Name the blood parasite species.
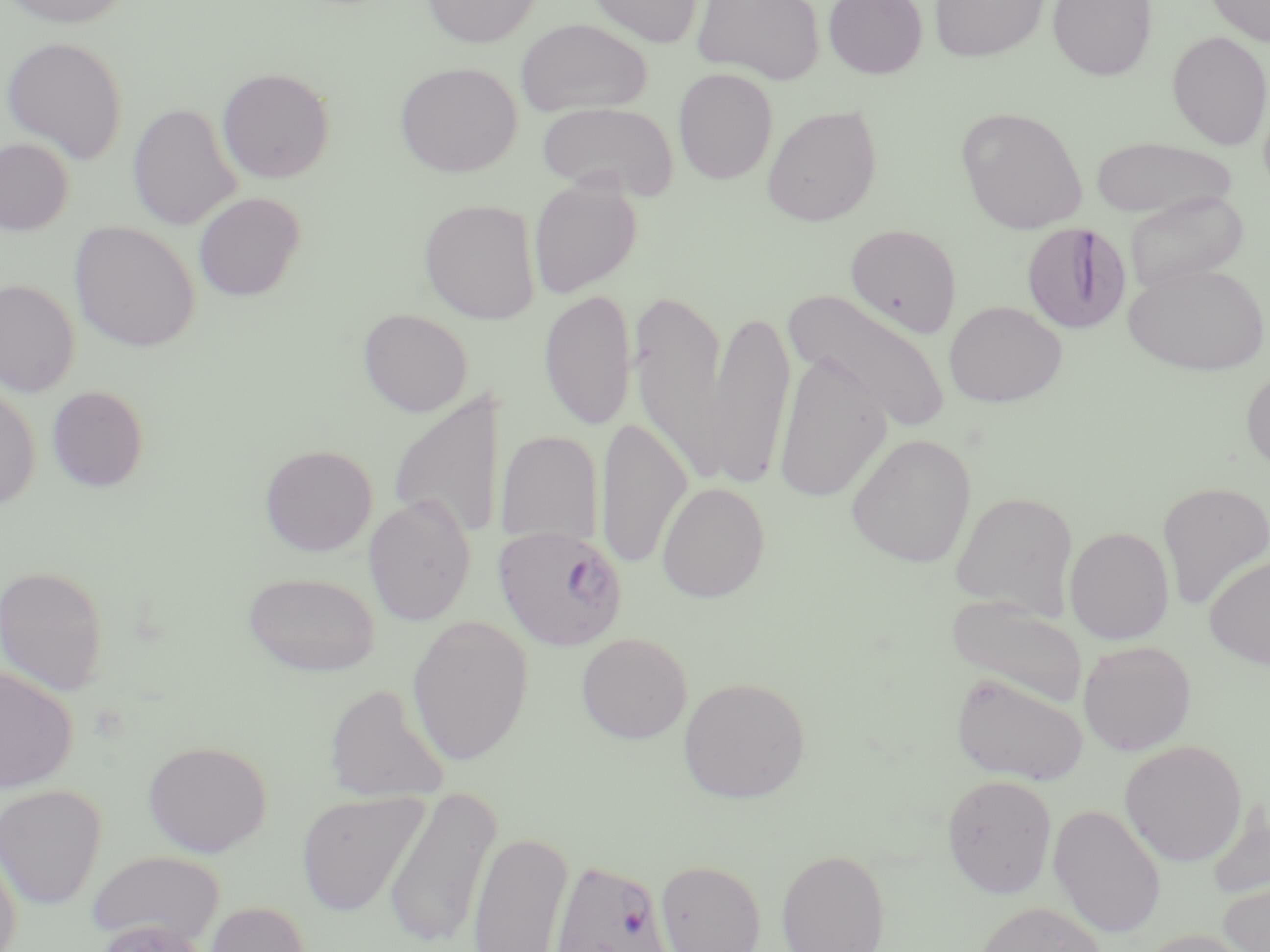
Plasmodium falciparum.

Summary:
  - Coordinate format: approximate bounding boxes as named x1/y1/x2/y2 corners in pixels
  - Uninfected red blood cell locations: (x1=0, y1=0, x2=134, y2=28), (x1=421, y1=0, x2=540, y2=48), (x1=584, y1=0, x2=704, y2=48), (x1=692, y1=0, x2=826, y2=84), (x1=823, y1=0, x2=928, y2=79), (x1=929, y1=0, x2=1049, y2=62), (x1=1048, y1=0, x2=1157, y2=81), (x1=1206, y1=0, x2=1270, y2=48), (x1=516, y1=18, x2=652, y2=117), (x1=1166, y1=31, x2=1270, y2=150), (x1=1, y1=35, x2=129, y2=163), (x1=394, y1=61, x2=522, y2=177), (x1=217, y1=67, x2=335, y2=184), (x1=673, y1=68, x2=778, y2=185), (x1=535, y1=101, x2=679, y2=199), (x1=128, y1=102, x2=242, y2=231), (x1=761, y1=104, x2=882, y2=226), (x1=956, y1=107, x2=1089, y2=234), (x1=1089, y1=136, x2=1237, y2=219), (x1=0, y1=137, x2=74, y2=235), (x1=528, y1=177, x2=641, y2=298), (x1=1124, y1=190, x2=1248, y2=295), (x1=193, y1=192, x2=305, y2=301), (x1=419, y1=199, x2=541, y2=324), (x1=69, y1=222, x2=200, y2=352), (x1=845, y1=223, x2=962, y2=338), (x1=1123, y1=261, x2=1269, y2=376), (x1=0, y1=278, x2=80, y2=396), (x1=539, y1=288, x2=637, y2=433), (x1=784, y1=288, x2=953, y2=434), (x1=629, y1=289, x2=728, y2=481), (x1=944, y1=300, x2=1067, y2=406), (x1=709, y1=306, x2=794, y2=491), (x1=358, y1=308, x2=473, y2=416), (x1=773, y1=352, x2=891, y2=502), (x1=1241, y1=366, x2=1270, y2=476), (x1=0, y1=384, x2=40, y2=511), (x1=47, y1=385, x2=149, y2=492), (x1=388, y1=390, x2=507, y2=541), (x1=596, y1=415, x2=692, y2=573), (x1=495, y1=430, x2=604, y2=548), (x1=846, y1=434, x2=976, y2=568), (x1=259, y1=444, x2=378, y2=556), (x1=1157, y1=481, x2=1270, y2=610), (x1=657, y1=482, x2=770, y2=602), (x1=950, y1=491, x2=1078, y2=617), (x1=364, y1=495, x2=476, y2=626), (x1=1065, y1=526, x2=1174, y2=644), (x1=1204, y1=554, x2=1270, y2=669), (x1=0, y1=565, x2=109, y2=696), (x1=243, y1=571, x2=380, y2=677), (x1=947, y1=595, x2=1087, y2=708), (x1=407, y1=614, x2=534, y2=767), (x1=575, y1=632, x2=693, y2=743), (x1=1078, y1=640, x2=1196, y2=756), (x1=0, y1=665, x2=79, y2=793), (x1=950, y1=671, x2=1089, y2=785), (x1=678, y1=677, x2=811, y2=804), (x1=323, y1=683, x2=451, y2=802), (x1=1120, y1=739, x2=1248, y2=867), (x1=142, y1=740, x2=272, y2=857), (x1=941, y1=773, x2=1058, y2=899), (x1=0, y1=784, x2=107, y2=909), (x1=383, y1=785, x2=501, y2=950), (x1=296, y1=791, x2=429, y2=916), (x1=1206, y1=802, x2=1270, y2=905), (x1=1048, y1=803, x2=1167, y2=938), (x1=467, y1=830, x2=572, y2=951), (x1=0, y1=842, x2=22, y2=952), (x1=777, y1=848, x2=891, y2=952), (x1=88, y1=849, x2=226, y2=943), (x1=655, y1=859, x2=765, y2=952), (x1=1219, y1=880, x2=1270, y2=952), (x1=975, y1=900, x2=1108, y2=952), (x1=205, y1=901, x2=312, y2=952), (x1=1135, y1=929, x2=1259, y2=952)
  - Plasmodium falciparum-infected red blood cell locations: (x1=1022, y1=222, x2=1131, y2=334), (x1=492, y1=524, x2=629, y2=651), (x1=553, y1=860, x2=670, y2=952)
  - Image size: 1270×952 pixels
  - Field of view: one of a larger specimen
  - Modality: optical microscopy
  - Preparation: thin blood film
  - Magnification: 1000x
  - Stain: May-Grünwald-Giemsa